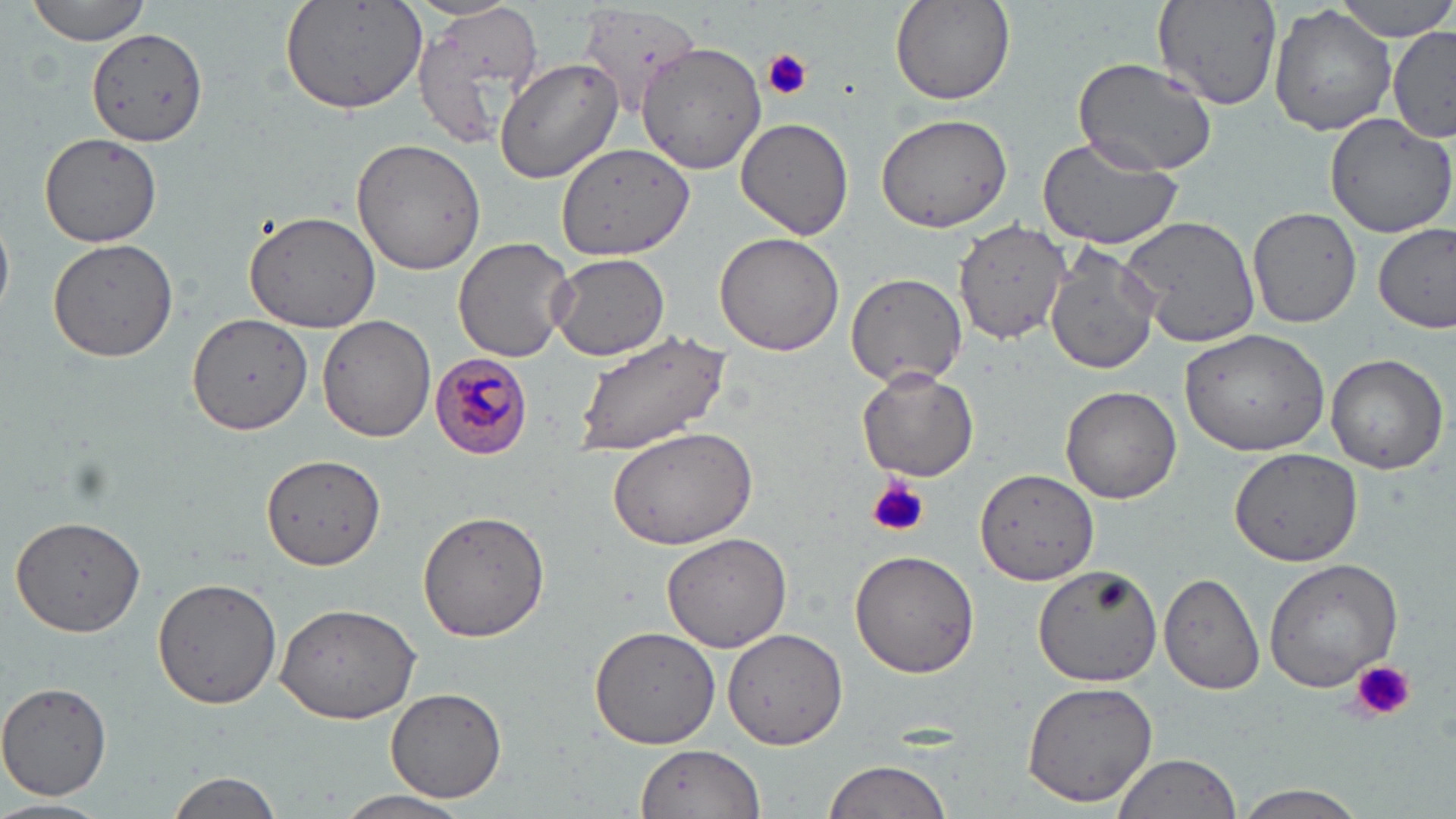

Summary:
  - Coordinate format: approximate bounding boxes as named x1/y1/x2/y2 corners in pixels
  - Uninfected red blood cell locations: (x1=26, y1=0, x2=153, y2=44), (x1=278, y1=0, x2=431, y2=114), (x1=888, y1=0, x2=1014, y2=107), (x1=1336, y1=0, x2=1456, y2=42), (x1=1151, y1=1, x2=1282, y2=110), (x1=1269, y1=4, x2=1397, y2=136), (x1=413, y1=5, x2=546, y2=153), (x1=86, y1=27, x2=207, y2=147), (x1=1390, y1=27, x2=1455, y2=141), (x1=635, y1=41, x2=769, y2=175), (x1=1073, y1=58, x2=1218, y2=176), (x1=497, y1=59, x2=623, y2=183), (x1=873, y1=112, x2=1014, y2=232), (x1=1324, y1=114, x2=1456, y2=241), (x1=735, y1=118, x2=854, y2=240), (x1=39, y1=133, x2=163, y2=247), (x1=1035, y1=134, x2=1182, y2=250), (x1=353, y1=136, x2=486, y2=275), (x1=557, y1=142, x2=695, y2=262), (x1=1247, y1=206, x2=1364, y2=329), (x1=243, y1=210, x2=382, y2=334), (x1=1122, y1=212, x2=1260, y2=349), (x1=955, y1=217, x2=1070, y2=344), (x1=0, y1=219, x2=13, y2=322), (x1=1375, y1=221, x2=1456, y2=333), (x1=713, y1=231, x2=843, y2=357), (x1=453, y1=236, x2=575, y2=363), (x1=47, y1=239, x2=178, y2=362), (x1=1044, y1=247, x2=1160, y2=379), (x1=548, y1=253, x2=669, y2=362), (x1=845, y1=272, x2=967, y2=388), (x1=189, y1=313, x2=312, y2=434), (x1=318, y1=316, x2=435, y2=442), (x1=1179, y1=327, x2=1329, y2=454), (x1=570, y1=329, x2=735, y2=456), (x1=1324, y1=352, x2=1449, y2=474), (x1=856, y1=366, x2=979, y2=480), (x1=1059, y1=386, x2=1182, y2=503), (x1=606, y1=424, x2=761, y2=551), (x1=1230, y1=448, x2=1364, y2=567), (x1=260, y1=453, x2=384, y2=570), (x1=975, y1=467, x2=1099, y2=586), (x1=417, y1=511, x2=550, y2=644), (x1=10, y1=513, x2=147, y2=638), (x1=660, y1=533, x2=792, y2=651), (x1=849, y1=550, x2=981, y2=679), (x1=1262, y1=557, x2=1406, y2=691), (x1=1036, y1=565, x2=1162, y2=687), (x1=152, y1=576, x2=282, y2=709), (x1=1159, y1=576, x2=1264, y2=694), (x1=274, y1=603, x2=422, y2=723), (x1=589, y1=624, x2=724, y2=750), (x1=723, y1=628, x2=851, y2=751), (x1=1021, y1=679, x2=1161, y2=808), (x1=0, y1=681, x2=113, y2=802), (x1=385, y1=688, x2=508, y2=802), (x1=634, y1=745, x2=767, y2=818), (x1=1110, y1=753, x2=1244, y2=819), (x1=821, y1=759, x2=951, y2=819), (x1=166, y1=770, x2=287, y2=819), (x1=1234, y1=785, x2=1370, y2=819), (x1=334, y1=790, x2=475, y2=819), (x1=0, y1=797, x2=109, y2=819)
  - Plasmodium malariae-infected red blood cell locations: (x1=429, y1=352, x2=534, y2=459)
  - Platelet locations: (x1=762, y1=48, x2=811, y2=101), (x1=868, y1=477, x2=929, y2=538), (x1=1353, y1=660, x2=1416, y2=722)
  - Slide-level diagnosis: Plasmodium malariae
  - Preparation: thin blood film
  - Image size: 1456×819 pixels
  - Field of view: one of a larger specimen
  - Modality: light microscopy
  - Magnification: 1000x
  - Stain: May-Grünwald-Giemsa